Give the extent of all Plasmodium falciparum-infected red blood cells.
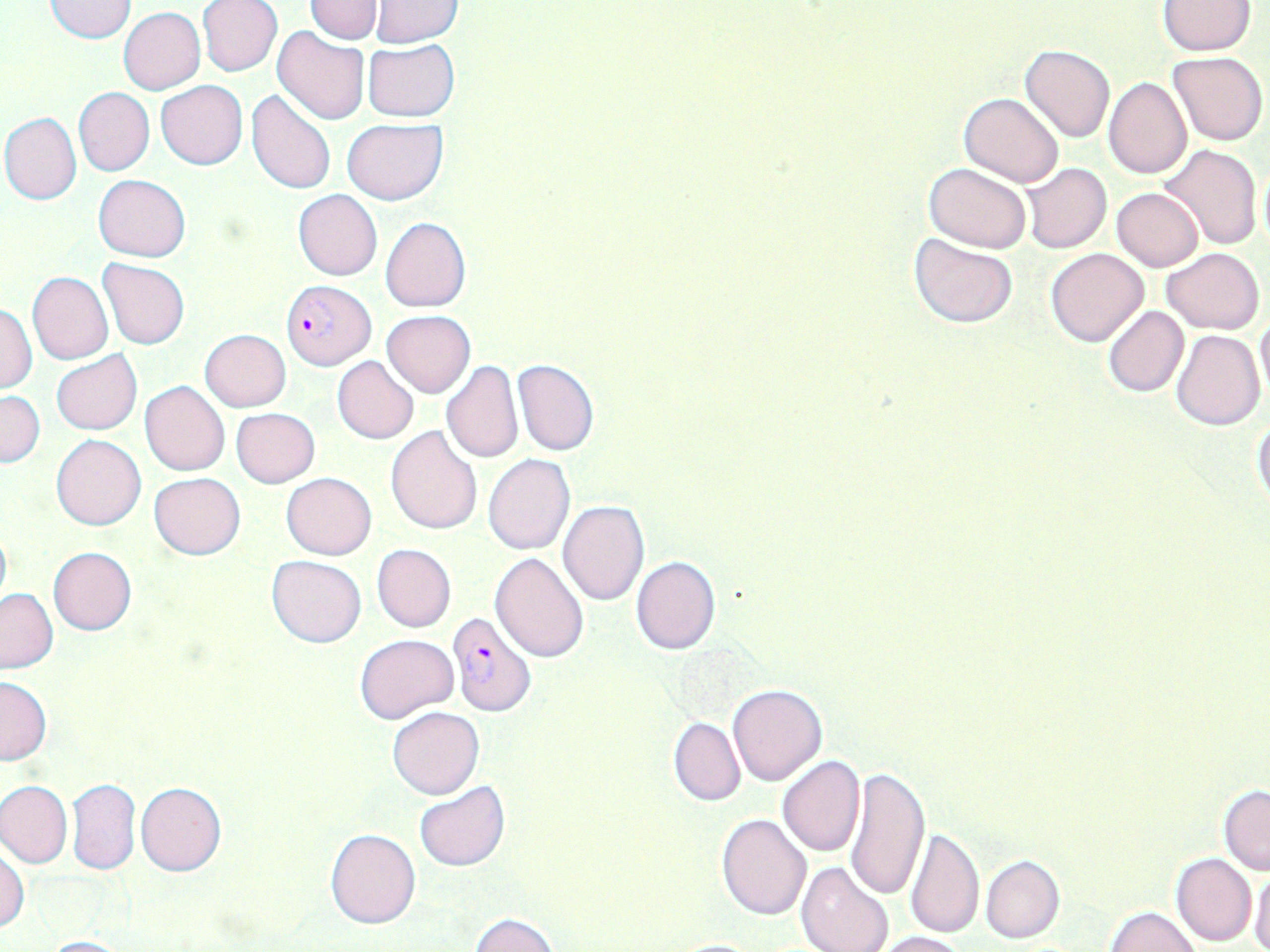

Approximate bounding boxes as (x1, y1, x2, y2) in pixels.
Plasmodium falciparum-infected red blood cells: (282, 278, 374, 369), (446, 610, 537, 719).

slide-level diagnosis = Plasmodium falciparum
stain = May-Grünwald-Giemsa
modality = light microscopy
uninfected red blood cell locations = approximate bounding boxes as (x1, y1, x2, y2) in pixels: (198, 0, 282, 76), (306, 0, 383, 43), (46, 1, 135, 43), (369, 1, 464, 47), (1157, 1, 1255, 55), (119, 9, 205, 93), (273, 26, 370, 125), (363, 39, 458, 122), (1020, 45, 1114, 143), (1167, 51, 1267, 146), (1103, 77, 1192, 180), (156, 81, 247, 169), (74, 87, 154, 176), (247, 89, 335, 192), (959, 92, 1065, 186), (1, 112, 81, 204), (343, 119, 447, 204), (1161, 144, 1264, 250), (1257, 159, 1269, 256), (925, 163, 1032, 253), (1022, 163, 1111, 254), (93, 175, 191, 261), (1112, 187, 1204, 271), (292, 189, 382, 281), (380, 217, 470, 312), (909, 233, 1016, 328), (1162, 246, 1264, 334), (1046, 248, 1149, 347), (97, 258, 190, 349), (27, 272, 113, 364), (1, 303, 37, 395), (1102, 306, 1188, 399), (382, 310, 475, 397), (1255, 311, 1270, 404), (1171, 328, 1265, 429), (200, 329, 291, 411), (52, 351, 141, 435), (332, 357, 418, 445), (512, 360, 600, 456), (441, 361, 523, 464), (140, 381, 231, 475), (0, 391, 44, 468), (232, 407, 319, 487), (1252, 416, 1270, 511), (386, 426, 481, 535), (52, 434, 146, 530), (483, 454, 575, 555), (148, 472, 245, 559), (282, 472, 377, 559), (557, 500, 650, 605), (0, 523, 11, 612), (372, 544, 456, 632), (48, 547, 137, 635), (491, 550, 589, 661), (265, 554, 366, 647), (630, 556, 720, 656), (0, 589, 57, 673), (355, 633, 459, 723), (0, 674, 51, 765), (727, 682, 829, 785), (388, 707, 484, 798), (669, 717, 745, 807), (778, 756, 865, 856), (845, 764, 929, 903), (0, 780, 72, 868), (67, 780, 141, 875), (415, 781, 510, 871), (136, 782, 226, 876), (1218, 784, 1270, 875), (718, 813, 813, 920), (906, 826, 985, 939), (325, 828, 420, 929), (0, 846, 28, 933), (1171, 853, 1257, 946), (980, 855, 1064, 943), (795, 861, 894, 952), (1250, 865, 1270, 952), (1105, 906, 1201, 952), (469, 912, 558, 952), (874, 931, 969, 952), (41, 936, 135, 952), (668, 938, 771, 952)
preparation = thin blood film
magnification = 1000x
field of view = one of a larger specimen
image size = 1270×952 pixels